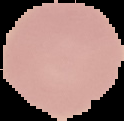

Summary:
  - Preparation: thin blood film
  - Result: no Plasmodium parasites detected
  - Image size: 124×121 pixels
  - Image type: cell region segmented out of the field of view; surrounding area masked to black